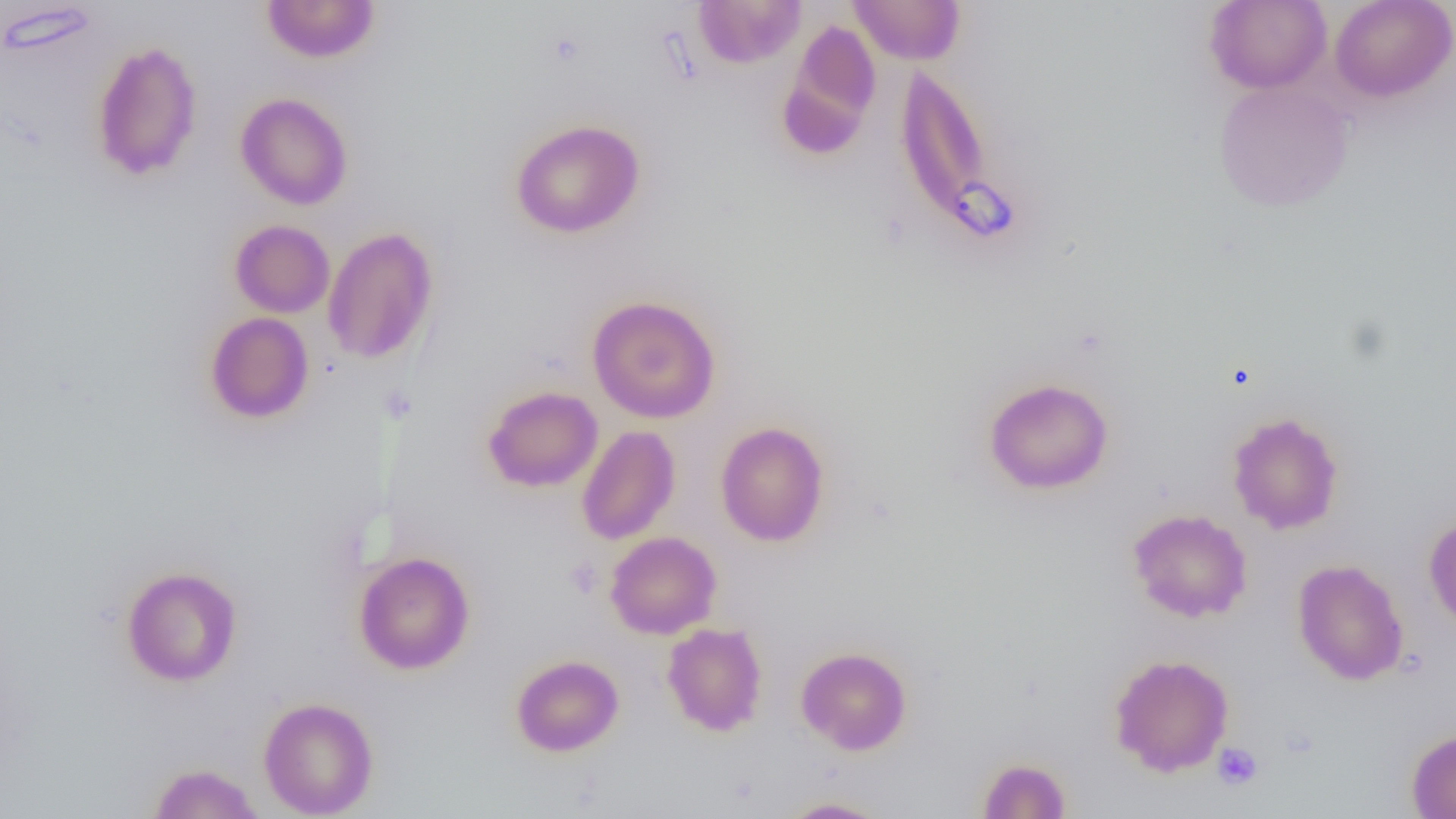
Approximate bounding boxes as (x1,y1)-(x2,y2) corner pairs in pixels. Platelet locations: (564,557)-(603,598), (1212,741)-(1263,791). Uninfected red blood cell locations: (261,0)-(381,63), (693,0)-(806,68), (849,0)-(965,65), (1329,0)-(1456,103), (1205,1)-(1332,94), (779,21)-(882,158), (91,40)-(203,181), (895,64)-(999,241), (1213,81)-(1353,212), (236,92)-(353,210), (511,119)-(645,238), (230,219)-(335,318), (322,226)-(438,366), (587,295)-(721,423), (205,312)-(314,424), (983,377)-(1113,495), (483,385)-(603,492), (1227,411)-(1344,535), (715,421)-(831,547), (576,425)-(681,545), (1127,508)-(1252,623), (1423,514)-(1456,634), (605,531)-(722,639), (353,551)-(475,674), (1292,559)-(1409,686), (122,566)-(241,686), (662,622)-(767,736), (796,646)-(912,754), (1109,653)-(1234,777), (511,654)-(624,756), (259,697)-(378,818), (1406,729)-(1456,818), (977,758)-(1072,818), (147,762)-(264,819), (778,796)-(892,818). Slide-level diagnosis: no evidence of blood parasites. Image is 1456×819 pixels. Captured at 1000x magnification. Optical microscopy. Single field of view. Thin blood film.